Comment on the morphology of the red blood cells.
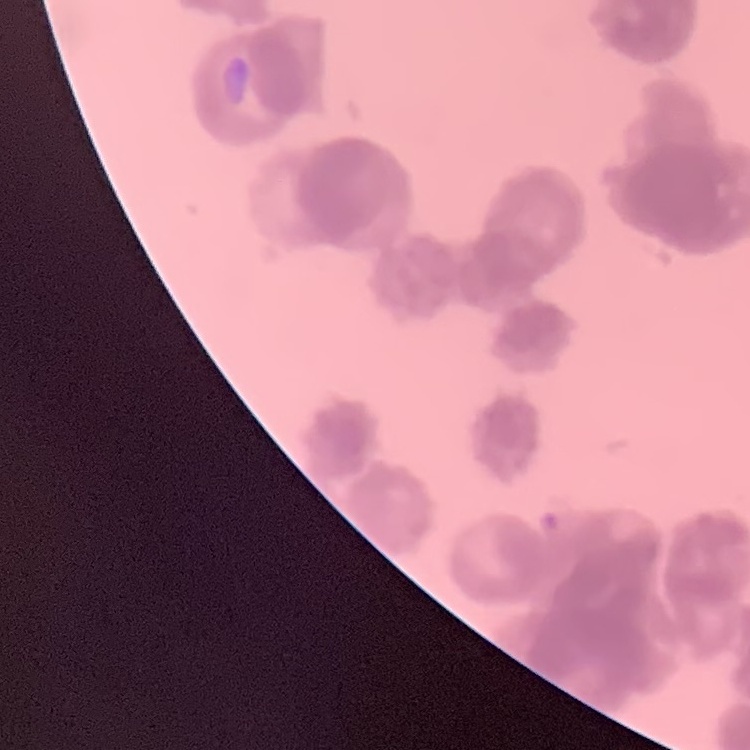

Rouleaux formation.

Summary:
  - Stain: Field's or Giemsa
  - Image type: one tile cut from a larger photomicrograph
  - Preparation: thin blood film